Identify the parasite.
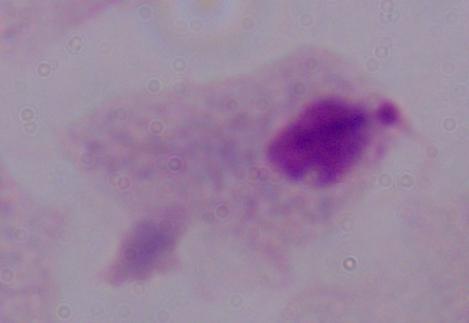

A trichomonad.

Summary:
  - Magnification: 1000x
  - Modality: photomicrograph